Evaluate for malaria.
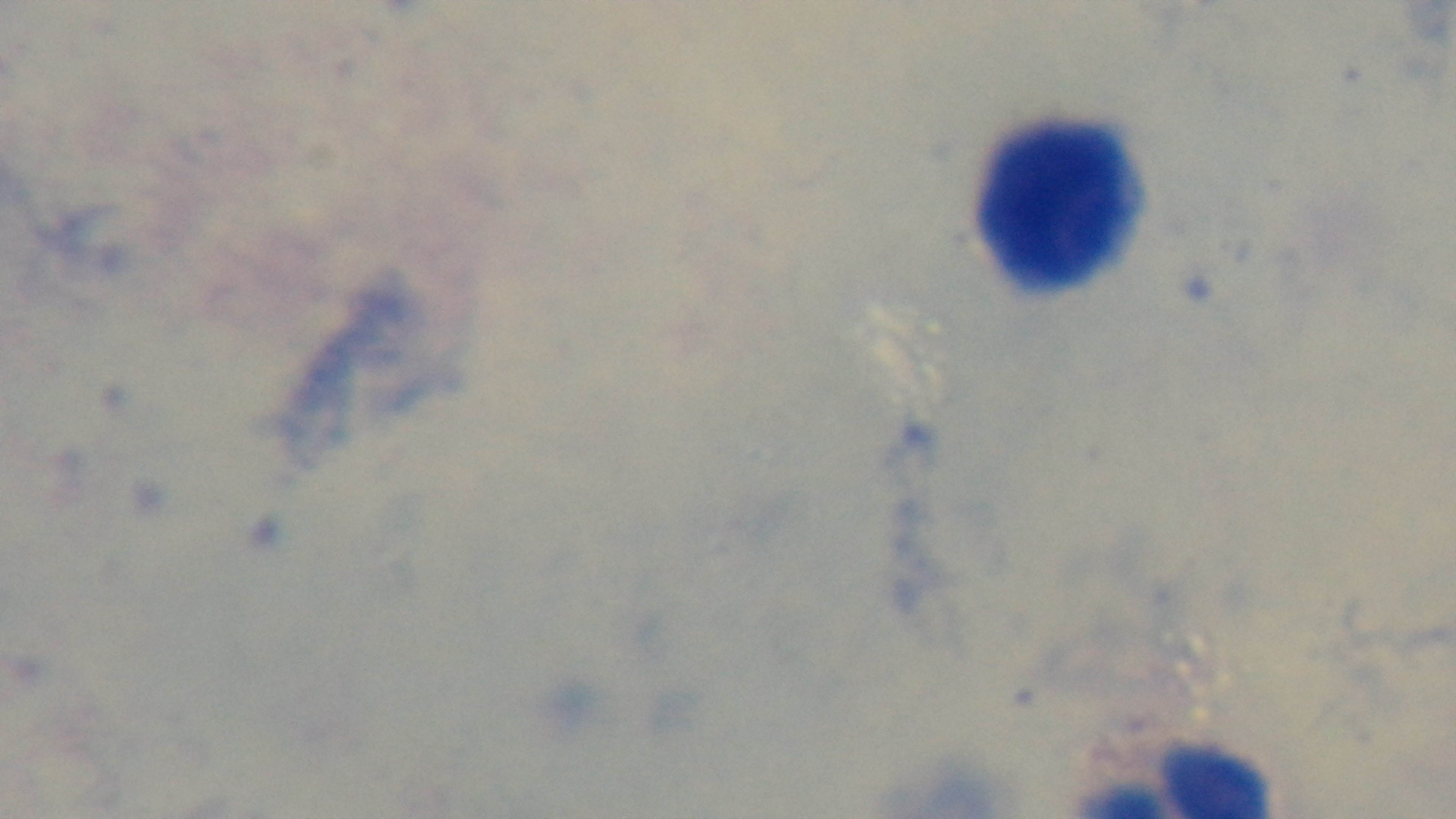
Negative.

Summary:
  - Objective: 100x oil immersion
  - Stain: Giemsa
  - Modality: light microscopy
  - Preparation: thick blood film
  - Capture: mounted 4K digital camera
  - Field of view: single